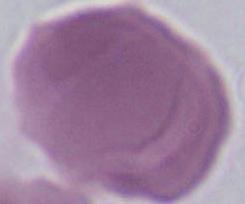
An erythrocyte is shown. Photomicrograph. Captured at 1000x magnification.